Classify this cell by malaria status.
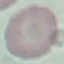

It is uninfected.

Thin blood smear. Giemsa-stained preparation. Acquired by smartphone through the microscope eyepiece. Automatically extracted cell patch, resized to 64 × 64 pixels.